Name the cell type shown.
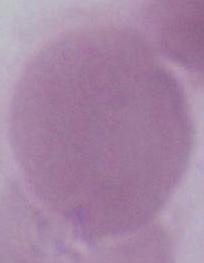

An erythrocyte.

magnification = 1000x
modality = micrograph